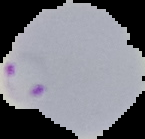

image_type: segmented cell region with the area outside set to black
image_size: 145×139 pixels
preparation: thin blood smear
malaria_status: parasitized